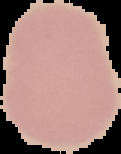

Segmented cell region on a black background. From a thin blood film. Image is 121×154 pixels. Result: no Plasmodium parasites detected.